Name the parasite shown.
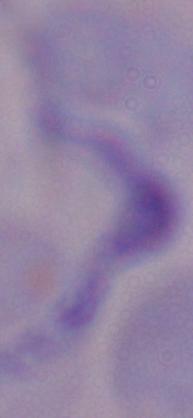

A trypanosome.

Micrograph. Captured at 1000x magnification.